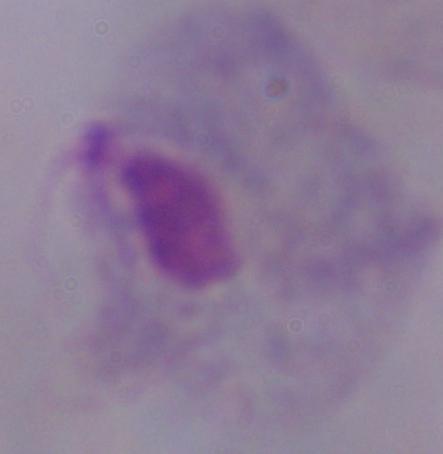

magnification = 1000x
identification = trichomonad
modality = photomicrograph